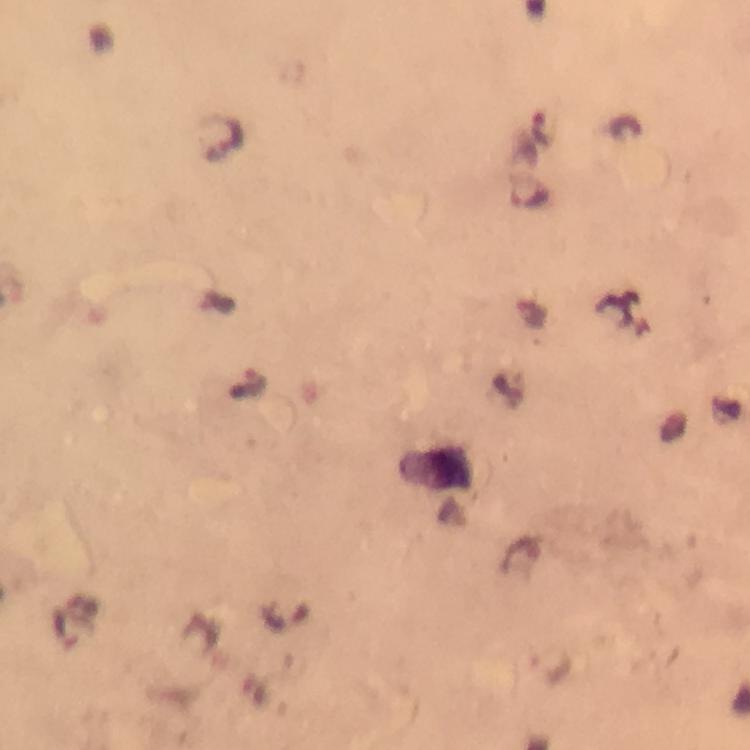

{
  "magnification": "100x",
  "immersion_oil": "applied",
  "image_size": "750×750 pixels",
  "plasmodium_parasite_locations": "approximate object centers, in pixels from the top-left corner: (x=544, y=130), (x=224, y=134), (x=529, y=194), (x=550, y=669)",
  "capture": "smartphone mounted on the microscope",
  "stain": "Giemsa",
  "preparation": "thick blood smear",
  "cropped_from": "a single field of view",
  "context": "from a malaria diagnostic workup"
}